Assess this cell for malaria.
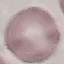

Uninfected.

Summary:
  - Image type: automatically extracted cell patch, resized to 64 × 64 pixels
  - Preparation: thin smear
  - Stain: Giemsa
  - Capture: smartphone through the microscope eyepiece